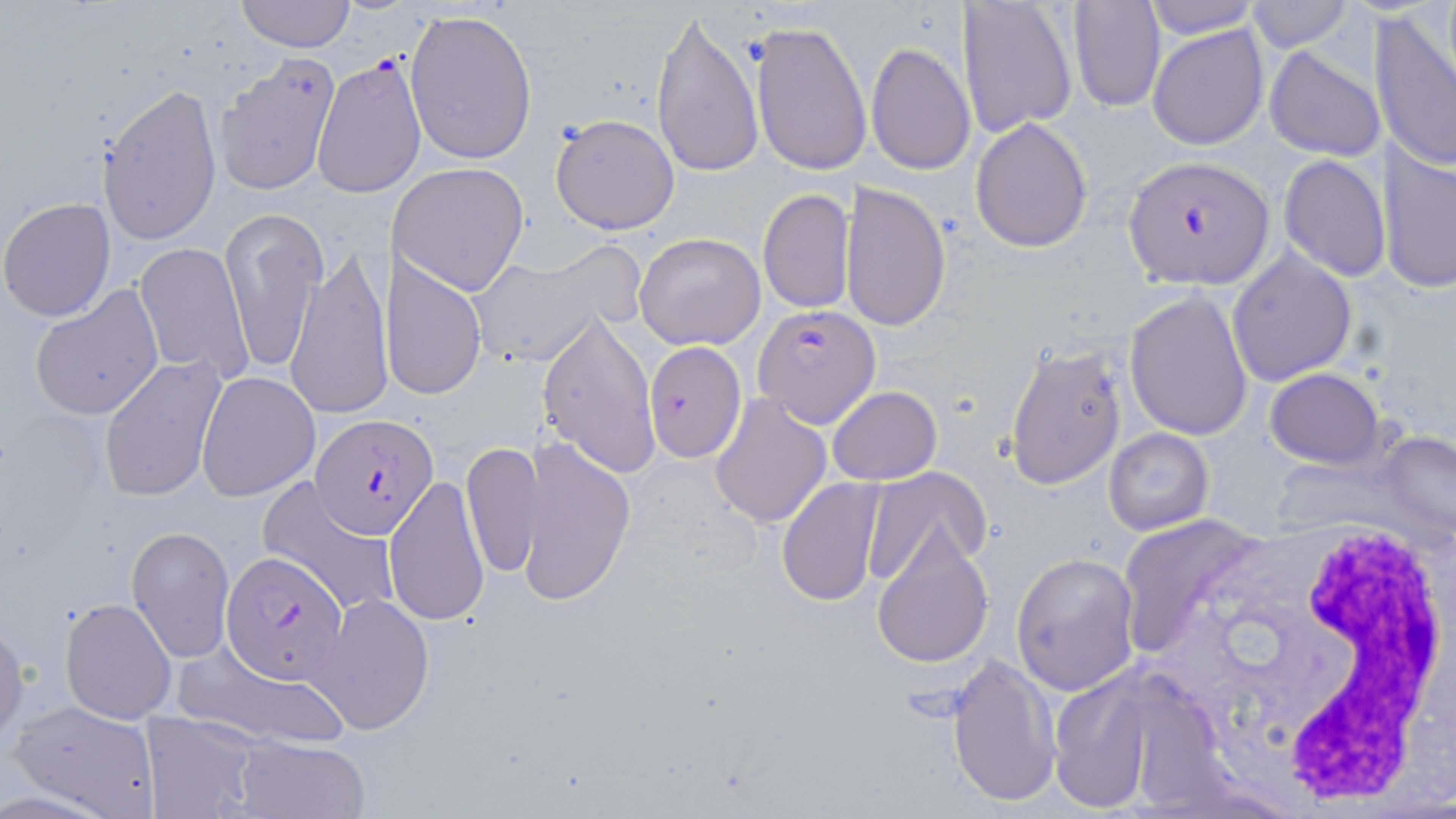

{
  "plasmodium_falciparum_infected_red_blood_cell_locations": "approximate bounding boxes as (x1,y1)-(x2,y2) corner pairs in pixels: (311,54)-(426,199), (1123,157)-(1274,287), (752,305)-(879,425), (312,416)-(437,535), (222,550)-(350,685)",
  "slide_level_diagnosis": "Plasmodium falciparum",
  "modality": "optical microscopy",
  "field_of_view": "one of a larger specimen",
  "uninfected_red_blood_cell_locations": "approximate bounding boxes as (x1,y1)-(x2,y2) corner pairs in pixels: (1139,0)-(1262,39), (236,1)-(357,51), (956,1)-(1077,140), (1244,1)-(1354,53), (1066,2)-(1165,112), (404,8)-(537,167), (1369,8)-(1456,173), (650,9)-(763,179), (749,18)-(872,174), (1147,23)-(1268,151), (866,41)-(975,176), (1263,46)-(1384,161), (215,54)-(342,196), (95,82)-(220,246), (550,114)-(678,235), (968,116)-(1091,253), (1378,140)-(1456,296), (1279,153)-(1390,281), (391,162)-(530,296), (844,182)-(950,335), (756,188)-(855,314), (1,198)-(116,322), (222,207)-(324,379), (634,232)-(765,349), (133,240)-(253,383), (469,246)-(634,372), (288,247)-(393,420), (1228,248)-(1356,387), (382,251)-(489,401), (29,286)-(165,420), (1124,289)-(1256,440), (538,312)-(661,477), (643,340)-(749,464), (1003,341)-(1129,491), (99,354)-(227,503), (1265,368)-(1383,468), (196,370)-(320,502), (827,386)-(943,485), (709,393)-(833,530), (1101,427)-(1215,535), (1378,432)-(1455,540), (463,440)-(546,581), (519,441)-(635,606), (862,466)-(991,585), (381,476)-(490,627), (776,476)-(889,607), (260,481)-(399,616), (1119,515)-(1264,660), (127,527)-(234,662), (872,527)-(994,668), (1011,553)-(1140,694), (312,592)-(434,736), (60,597)-(177,724), (0,619)-(27,747), (173,642)-(352,749), (947,652)-(1061,809), (1048,669)-(1166,815), (9,700)-(162,817), (142,711)-(260,819), (234,736)-(369,819)",
  "white_blood_cell_locations": "approximate bounding boxes as (x1,y1)-(x2,y2) corner pairs in pixels: (1148,514)-(1456,804)",
  "preparation": "thin blood smear",
  "magnification": "1000x",
  "stain": "May-Grünwald-Giemsa",
  "image_size": "1456×819 pixels"
}